Locate and identify every blood parasite.
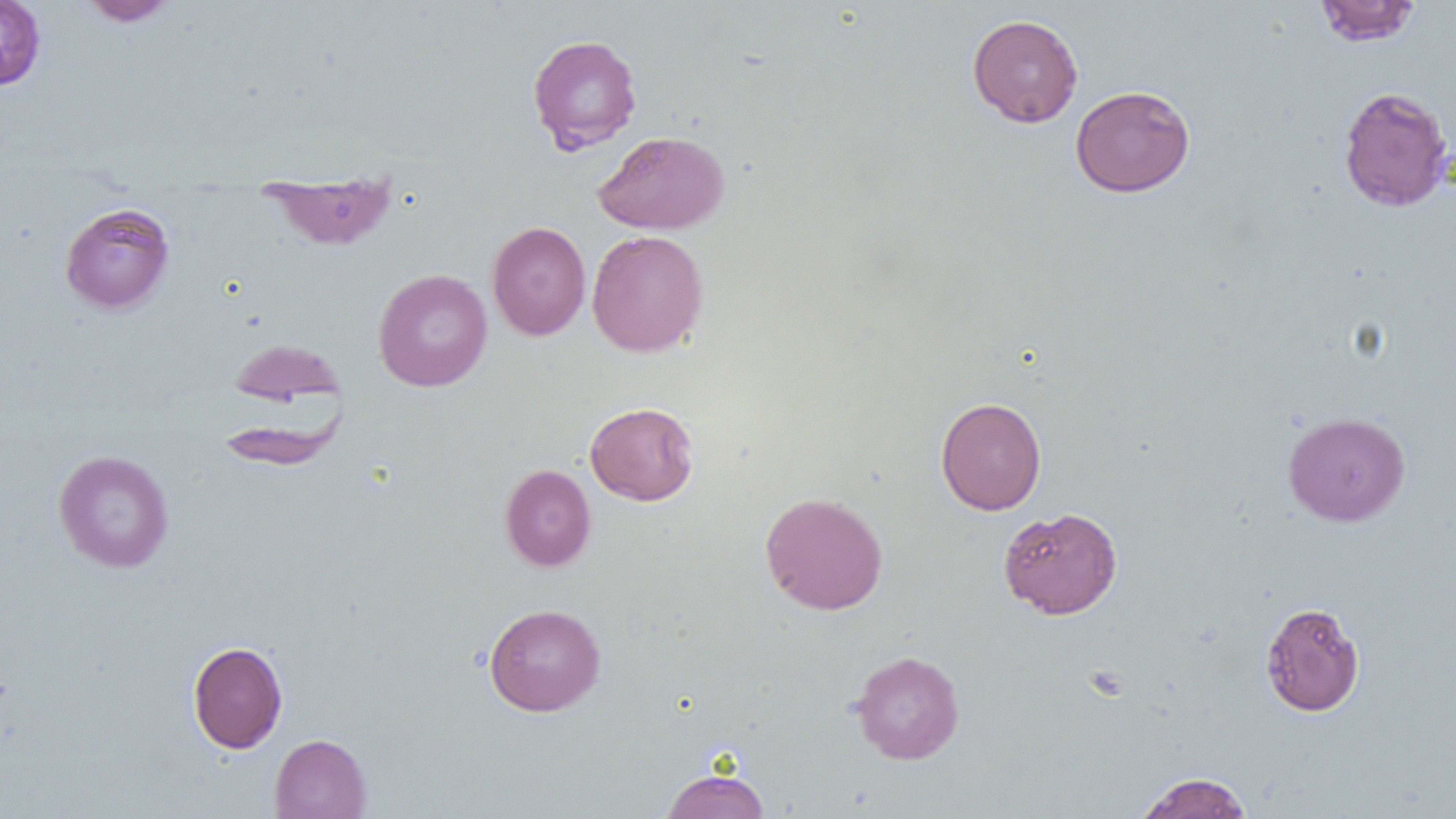

No blood parasites seen.

slide_level_diagnosis: negative for blood parasites
preparation: thin blood smear
modality: light microscopy
uninfected_red_blood_cell_locations: 'approximate bounding boxes as named x1/y1/x2/y2 corners in pixels: (x1=0, y1=0, x2=46, y2=90), (x1=79, y1=0, x2=178, y2=26), (x1=1314, y1=1, x2=1421, y2=46), (x1=966, y1=14, x2=1083, y2=127), (x1=527, y1=34, x2=643, y2=153), (x1=1070, y1=85, x2=1195, y2=197), (x1=1338, y1=85, x2=1453, y2=212), (x1=593, y1=130, x2=730, y2=234), (x1=260, y1=170, x2=398, y2=251), (x1=59, y1=202, x2=175, y2=314), (x1=487, y1=221, x2=591, y2=341), (x1=586, y1=230, x2=709, y2=357), (x1=373, y1=268, x2=492, y2=392), (x1=226, y1=338, x2=346, y2=409), (x1=935, y1=396, x2=1047, y2=515), (x1=584, y1=401, x2=699, y2=506), (x1=1282, y1=411, x2=1410, y2=526), (x1=53, y1=449, x2=175, y2=573), (x1=500, y1=464, x2=596, y2=571), (x1=759, y1=491, x2=889, y2=615), (x1=998, y1=506, x2=1123, y2=619), (x1=1260, y1=602, x2=1365, y2=716), (x1=483, y1=603, x2=606, y2=716), (x1=188, y1=641, x2=288, y2=753), (x1=850, y1=649, x2=965, y2=764), (x1=269, y1=733, x2=372, y2=819), (x1=660, y1=768, x2=769, y2=819), (x1=1134, y1=772, x2=1254, y2=819)'
magnification: 1000x
field_of_view: single
image_size: 1456×819 pixels